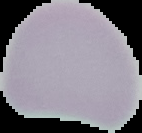

preparation: thin blood smear
image_type: segmented cell region with the area outside set to black
result: no Plasmodium parasites detected
image_size: 142×133 pixels